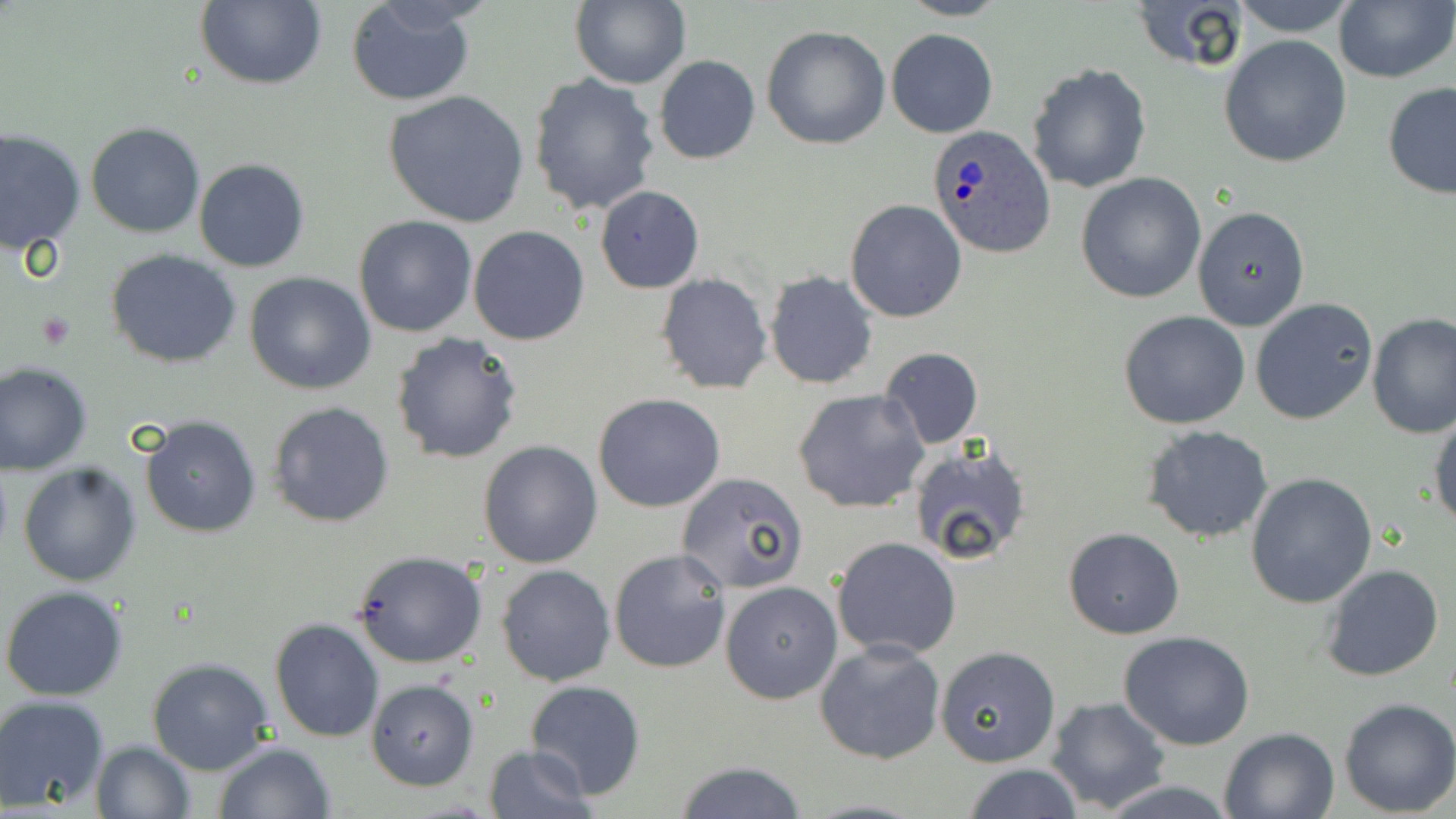 Approximate bounding boxes as (x1, y1, x2, y2) in pixels. Platelet locations: (35, 313, 75, 350). Uninfected red blood cell locations: (193, 0, 327, 89), (571, 0, 690, 90), (896, 0, 1009, 22), (1128, 0, 1251, 74), (1227, 0, 1361, 37), (1334, 0, 1455, 83), (345, 1, 477, 107), (762, 25, 892, 150), (885, 29, 998, 139), (1219, 36, 1352, 170), (654, 56, 760, 165), (1025, 63, 1151, 193), (529, 73, 660, 215), (1381, 82, 1456, 200), (382, 90, 529, 229), (86, 123, 205, 238), (0, 127, 86, 252), (193, 158, 310, 272), (1076, 171, 1206, 303), (595, 185, 704, 293), (844, 198, 966, 323), (1193, 206, 1309, 330), (352, 216, 478, 337), (468, 226, 591, 345), (106, 249, 241, 368), (764, 271, 879, 390), (244, 272, 375, 394), (655, 273, 773, 394), (1250, 299, 1378, 426), (1118, 311, 1250, 429), (1366, 314, 1456, 440), (390, 331, 526, 465), (879, 345, 984, 447), (0, 359, 94, 476), (793, 388, 931, 514), (593, 393, 727, 512), (266, 400, 396, 528), (1429, 411, 1456, 531), (140, 415, 264, 538), (1141, 424, 1274, 543), (478, 441, 603, 568), (909, 443, 1031, 568), (17, 461, 142, 588), (677, 472, 808, 594), (1246, 473, 1377, 609), (1063, 528, 1184, 640), (830, 536, 963, 661), (353, 549, 487, 668), (609, 549, 732, 674), (496, 563, 617, 685), (1318, 564, 1444, 683), (721, 581, 842, 704), (1, 585, 130, 699), (269, 617, 385, 743), (1119, 633, 1256, 750), (813, 637, 946, 765), (935, 645, 1061, 768), (146, 656, 274, 775), (525, 678, 646, 801), (365, 680, 478, 791), (0, 694, 111, 813), (1046, 697, 1172, 814), (1337, 698, 1456, 817), (1219, 726, 1341, 819), (90, 741, 196, 819), (213, 742, 335, 819), (481, 744, 597, 819), (673, 760, 808, 818), (962, 764, 1085, 819), (1092, 779, 1242, 817). Plasmodium ovale-infected red blood cell locations: (927, 126, 1056, 259). Slide-level diagnosis: Plasmodium ovale. Thin blood smear. Captured at 1000x magnification. Single field of view. May-Grünwald-Giemsa stain. Optical microscopy. Image is 1456×819 pixels.